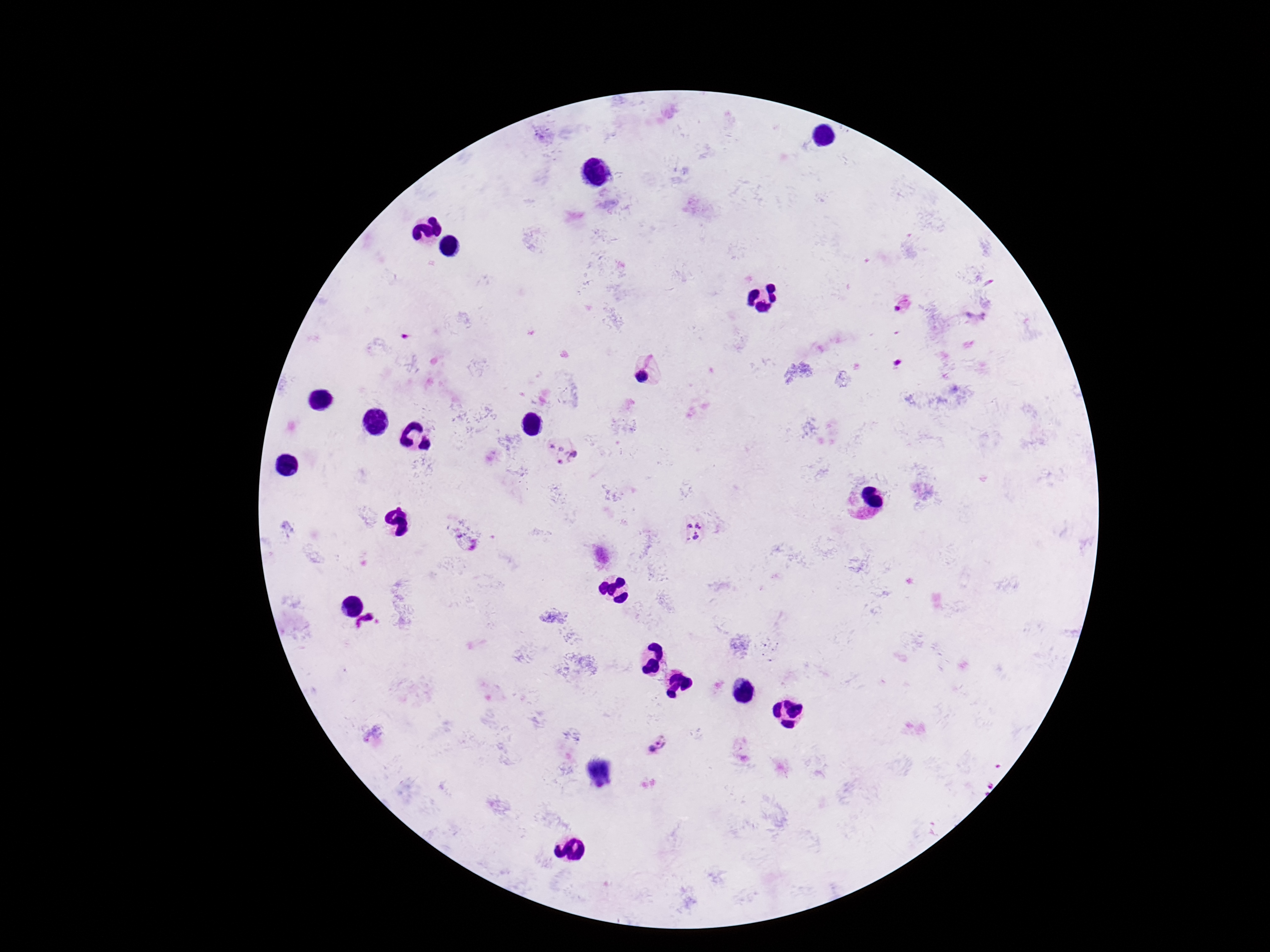

magnification: 100x
plasmodium_parasite_locations: 'approximate centers as (x, y) in pixels: (897, 308), (645, 371), (562, 452), (693, 530), (657, 744)'
preparation: thick blood smear
capture: smartphone camera through the microscope eyepiece
patient_malaria_status: infected
image_size: 1270×952 pixels
field_of_view: single
stain: Giemsa